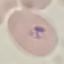 Result: malaria parasites identified. Cell patch, automatically extracted from a larger field of view and resized to 64 × 64 pixels. Giemsa stain. Acquired by smartphone through the microscope eyepiece. Thin blood smear.